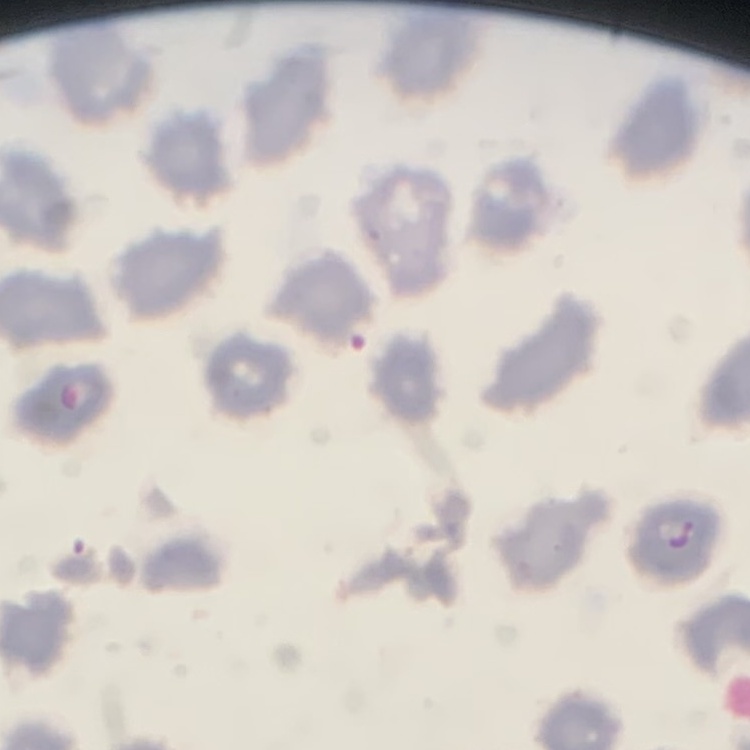
erythrocyte morphology = no rouleaux formation
stain = Field's or Giemsa
preparation = thin blood film
image type = square crop of a larger photomicrograph